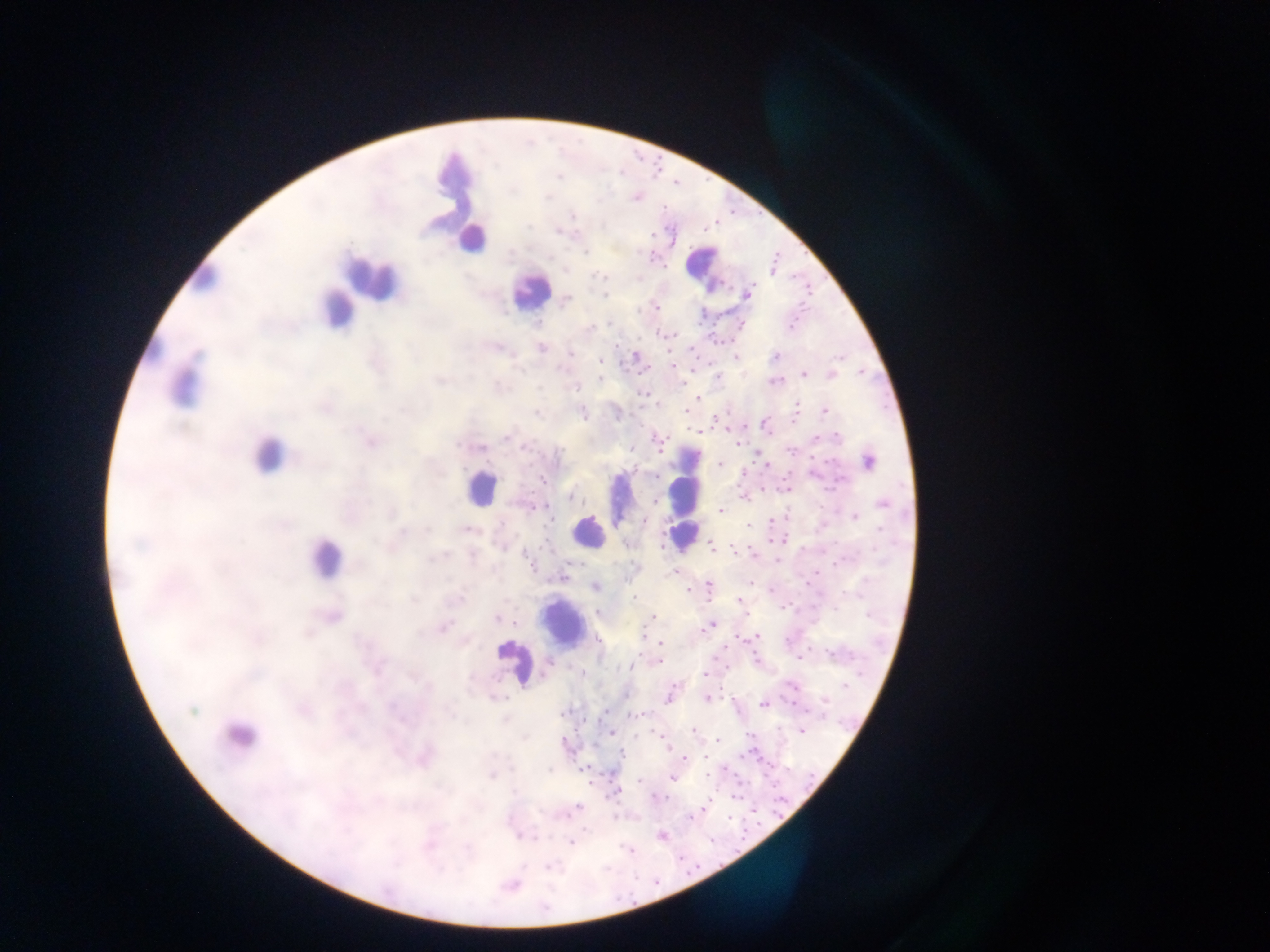
Approximate centers as [x, y] in pixels.
Summary:
  - Leukocyte locations: [455, 180], [463, 211], [471, 238], [703, 265], [202, 276], [370, 278], [530, 292], [337, 309], [184, 383], [267, 454], [685, 483], [481, 487], [616, 498], [588, 532], [679, 534], [324, 559], [562, 625], [513, 662], [239, 735]
  - Malaria parasite locations: [573, 215], [558, 232], [773, 268], [746, 294], [606, 296], [566, 299], [656, 308], [537, 323], [541, 349], [569, 352], [635, 356], [775, 356], [735, 357], [599, 361], [804, 375], [831, 375], [717, 377], [599, 379], [774, 381], [697, 399], [824, 411], [582, 412], [699, 430], [370, 440], [737, 444], [477, 448], [630, 449], [869, 460], [719, 464], [765, 465], [542, 480], [786, 487], [742, 497], [884, 504], [720, 510], [855, 517], [550, 518], [644, 521], [773, 521], [748, 525], [467, 530], [780, 540], [628, 544], [710, 545], [754, 554], [675, 572], [562, 576], [749, 581], [708, 584], [595, 587], [688, 590], [773, 590], [460, 599], [634, 599], [739, 599], [599, 612], [330, 615], [746, 615], [497, 617], [651, 617], [711, 624], [442, 627], [645, 635], [737, 636], [757, 637], [661, 642], [658, 661], [546, 663], [630, 666], [582, 673], [703, 675], [792, 684], [845, 685], [669, 697], [707, 698], [764, 704], [635, 714], [801, 730], [695, 731], [611, 733], [750, 735], [718, 741], [669, 748], [422, 756], [621, 756], [705, 757], [684, 758], [583, 767], [671, 777], [639, 780], [657, 797], [704, 807], [520, 835], [661, 835], [571, 842], [630, 851], [510, 885]
  - Image size: 1270×952 pixels
  - Preparation: thick blood film
  - Capture: mobile-phone photograph through a microscope
  - Country: Ghana
  - Field of view: single